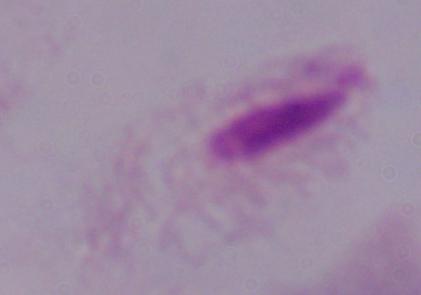

Summary:
  - Magnification: 1000x
  - Identification: trichomonad
  - Modality: photomicrograph